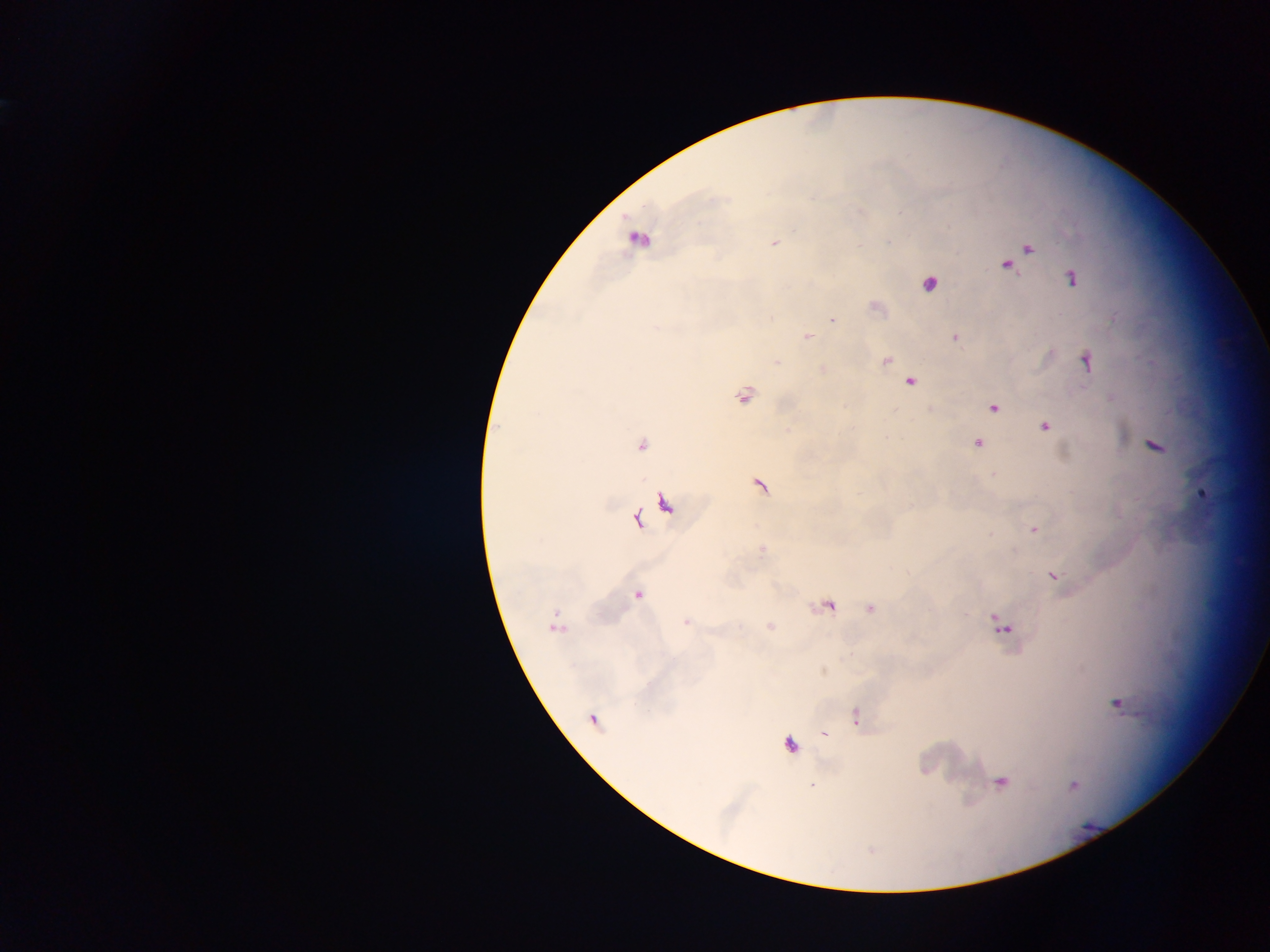

country = Ghana
preparation = thick blood film
Plasmodium parasite locations = approximate centers as {x, y} in pixels: {774, 243}, {1029, 248}, {1006, 265}, {1071, 279}, {930, 284}, {833, 320}, {807, 337}, {956, 338}, {887, 360}, {1086, 361}, {909, 382}, {745, 397}, {994, 408}, {1045, 426}, {978, 443}, {641, 444}, {1156, 445}, {760, 486}, {1203, 494}, {637, 519}, {1034, 530}, {762, 549}, {1054, 575}, {637, 594}, {871, 609}, {685, 622}, {1002, 625}, {1117, 705}, {856, 716}, {592, 720}, {824, 735}, {791, 745}, {1002, 783}, {811, 785}, {1074, 785}
image size = 1270×952 pixels
field of view = single
capture = mobile-phone photograph through a microscope
leukocyte locations = approximate centers as {x, y} in pixels: {639, 238}